Assess this cell for malaria.
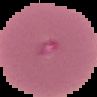

Uninfected.

preparation: thin blood film
image_size: 97×97 pixels
image_type: cell region segmented out of the field of view; surrounding area masked to black